Describe the morphology of the red blood cells.
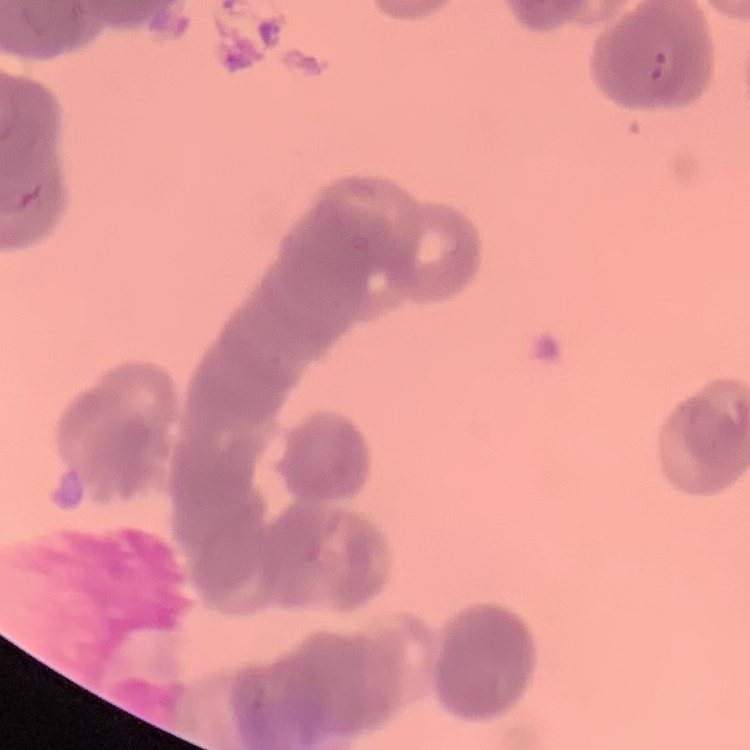

Rouleaux formation.

Summary:
  - Preparation: thin blood film
  - Stain: Field's or Giemsa
  - Image type: one tile cut from a larger photomicrograph